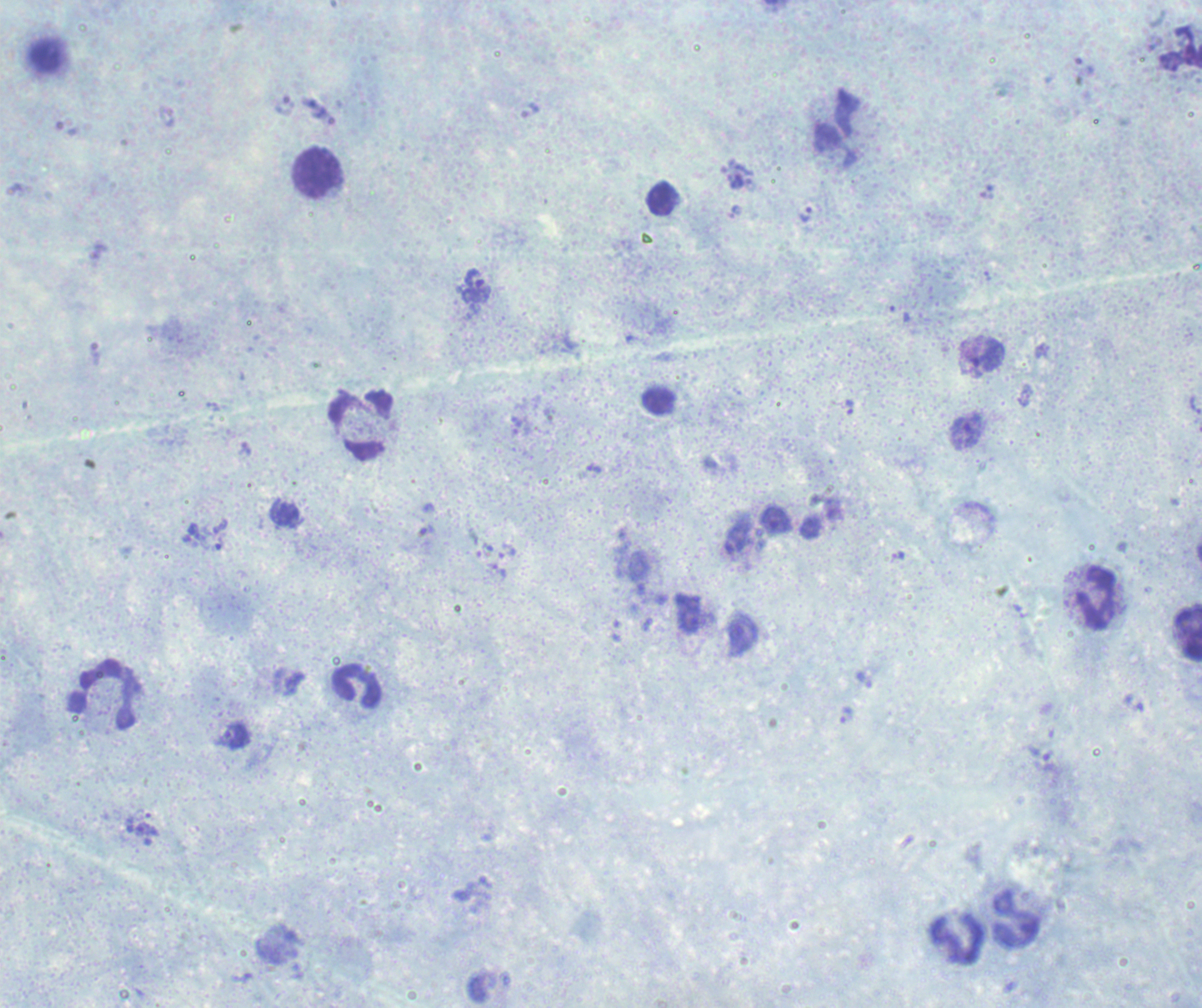
Romanowsky-stained preparation. Thick blood smear. One field from this slide. Image is 1202×1008 pixels.